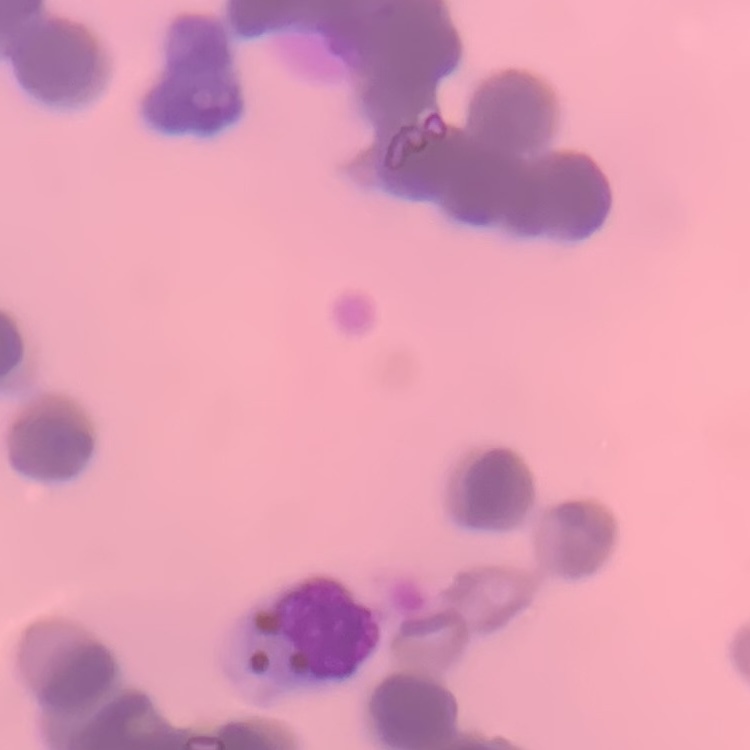
The erythrocytes show rouleaux formation. Thin blood smear. Square crop of a larger photomicrograph. Stained with either Field's or Giemsa.